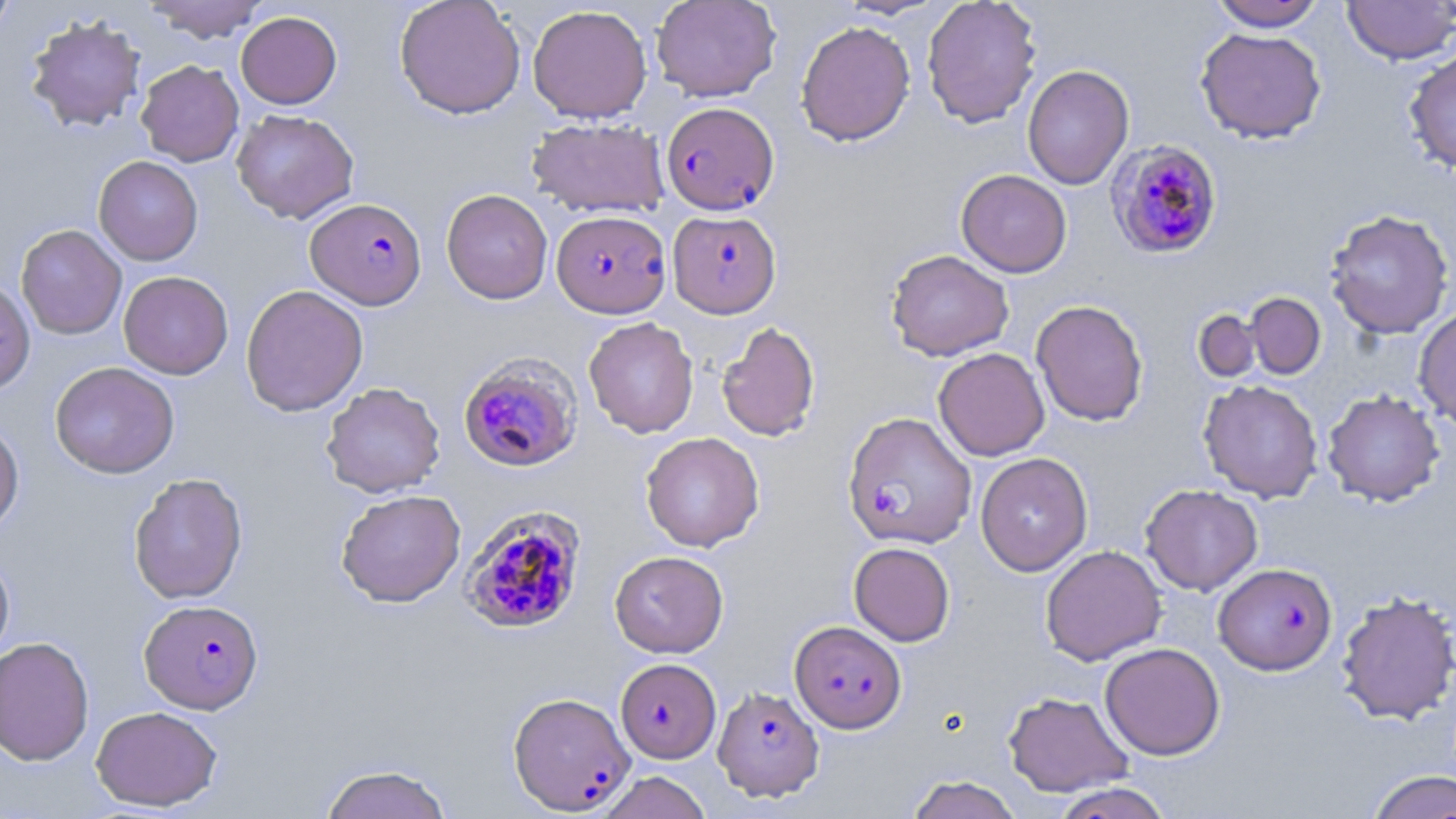

Summary:
  - Coordinate format: approximate bounding boxes as (x1,y1)-(x2,y2) corner pairs in pixels
  - Plasmodium falciparum-infected red blood cell locations: (660,101)-(779,216), (1108,140)-(1224,259), (306,198)-(427,310), (552,209)-(671,318), (668,209)-(782,318), (458,351)-(583,472), (843,411)-(976,548), (459,504)-(587,636), (1213,562)-(1337,675), (139,599)-(263,714), (789,620)-(906,733), (616,658)-(721,763), (713,685)-(824,800), (513,693)-(640,816)
  - Uninfected red blood cell locations: (0,0)-(17,41), (145,0)-(267,43), (394,0)-(526,119), (651,0)-(781,102), (834,0)-(950,20), (922,0)-(1042,129), (1209,1)-(1327,31), (1342,1)-(1455,65), (527,4)-(652,123), (236,11)-(341,109), (25,14)-(147,132), (796,20)-(915,146), (1195,27)-(1327,144), (1403,49)-(1456,176), (136,60)-(244,166), (1022,64)-(1134,190), (231,109)-(359,224), (526,117)-(669,218), (93,156)-(203,265), (956,169)-(1072,277), (441,189)-(553,304), (1324,208)-(1454,340), (16,224)-(127,340), (886,249)-(1014,361), (118,271)-(233,379), (0,279)-(36,396), (241,284)-(368,416), (1245,292)-(1326,379), (1031,299)-(1148,426), (1414,306)-(1456,431), (1193,310)-(1262,383), (584,316)-(699,438), (717,322)-(820,442), (933,348)-(1049,461), (49,361)-(180,479), (1198,379)-(1324,504), (321,381)-(445,498), (1322,390)-(1444,507), (0,419)-(24,538), (641,432)-(765,552), (975,452)-(1093,575), (129,472)-(248,604), (1141,484)-(1263,595), (336,489)-(465,607), (849,542)-(955,646), (1040,545)-(1166,666), (0,551)-(15,667), (610,551)-(729,657), (1336,589)-(1456,726), (0,636)-(94,766), (1099,642)-(1225,760), (1003,691)-(1133,797), (90,705)-(223,812), (318,763)-(453,819), (1366,769)-(1456,819), (595,771)-(714,819), (906,775)-(1022,819), (1051,782)-(1173,819)
  - Slide-level diagnosis: Plasmodium falciparum
  - Stain: May-Grünwald-Giemsa
  - Field of view: one of a larger specimen
  - Modality: light microscopy
  - Magnification: 1000x
  - Preparation: thin blood film
  - Image size: 1456×819 pixels